Report the malaria status of this cell.
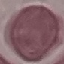

Uninfected.

Summary:
  - Capture: smartphone through the microscope eyepiece
  - Preparation: thin blood film
  - Stain: Giemsa
  - Image type: automatically extracted cell patch, resized to 64 × 64 pixels